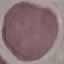 Malaria status: uninfected. Giemsa-stained preparation. Cell patch, automatically extracted from a larger field of view and resized to 64 × 64 pixels. Thin blood film. Acquired by smartphone through the microscope eyepiece.